Give the extent of the malaria parasites you find, grouped by life-cycle stage — ring form, trophozoite, schizont, or gametocyte.
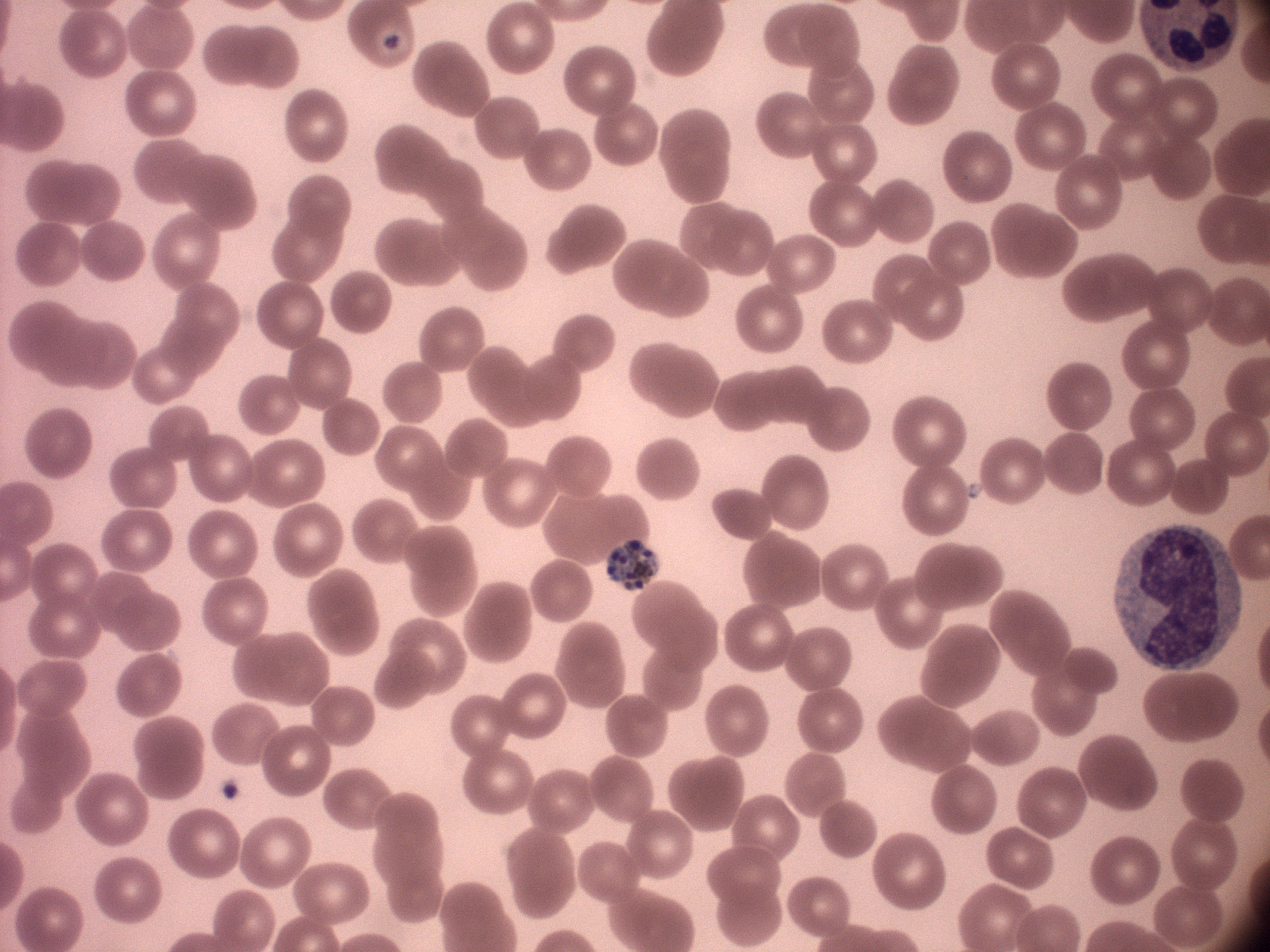
Approximate bounding boxes as (x1,y1)-(x2,y2) corner pairs in pixels, from the source annotation, which is not necessarily exhaustive.
Schizonts: (608,540)-(656,591).

field_of_view: one from this slide
stain: Giemsa
preparation: thin blood film
species: Plasmodium malariae
image_size: 1270×952 pixels
microscope: Leica DM2000 with built-in camera
magnification: 100x